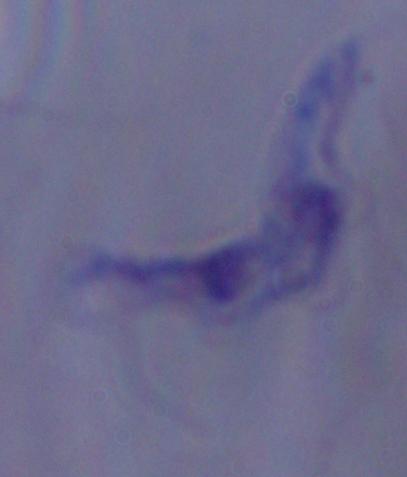

Summary:
  - Modality: photomicrograph
  - Identification: trypanosome
  - Magnification: 1000x